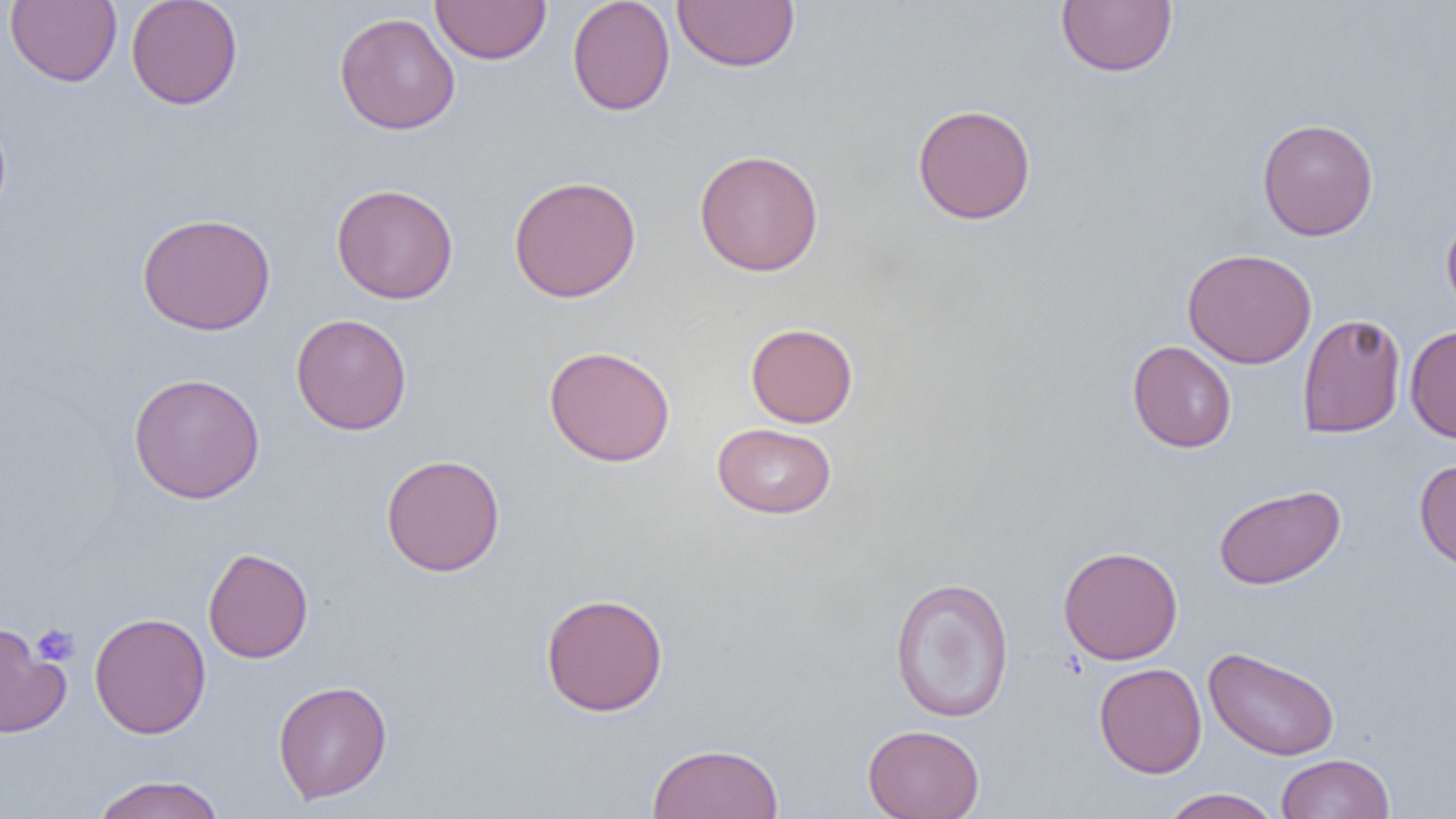
Summary:
  - Coordinate format: approximate bounding boxes as named x1/y1/x2/y2 corners in pixels
  - Uninfected red blood cell locations: (x1=5, y1=0, x2=122, y2=87), (x1=126, y1=0, x2=243, y2=110), (x1=430, y1=0, x2=551, y2=64), (x1=567, y1=0, x2=676, y2=116), (x1=672, y1=0, x2=800, y2=73), (x1=1056, y1=0, x2=1177, y2=77), (x1=334, y1=12, x2=460, y2=135), (x1=912, y1=103, x2=1037, y2=225), (x1=0, y1=110, x2=12, y2=226), (x1=1257, y1=118, x2=1379, y2=241), (x1=694, y1=149, x2=824, y2=276), (x1=508, y1=175, x2=642, y2=303), (x1=331, y1=184, x2=459, y2=304), (x1=1441, y1=208, x2=1456, y2=321), (x1=136, y1=212, x2=276, y2=335), (x1=1182, y1=248, x2=1317, y2=369), (x1=1297, y1=313, x2=1406, y2=438), (x1=290, y1=314, x2=412, y2=435), (x1=745, y1=322, x2=858, y2=428), (x1=1405, y1=325, x2=1456, y2=443), (x1=1127, y1=340, x2=1237, y2=453), (x1=544, y1=345, x2=675, y2=467), (x1=128, y1=372, x2=266, y2=504), (x1=712, y1=422, x2=837, y2=519), (x1=381, y1=454, x2=505, y2=577), (x1=1414, y1=458, x2=1456, y2=572), (x1=1213, y1=484, x2=1346, y2=590), (x1=1057, y1=545, x2=1184, y2=664), (x1=203, y1=547, x2=313, y2=663), (x1=889, y1=575, x2=1015, y2=723), (x1=540, y1=592, x2=669, y2=717), (x1=89, y1=612, x2=211, y2=739), (x1=0, y1=623, x2=70, y2=738), (x1=1204, y1=646, x2=1341, y2=761), (x1=1094, y1=663, x2=1206, y2=778), (x1=273, y1=680, x2=392, y2=804), (x1=862, y1=724, x2=985, y2=819), (x1=646, y1=742, x2=784, y2=819), (x1=1276, y1=753, x2=1395, y2=819), (x1=91, y1=774, x2=226, y2=819), (x1=1159, y1=788, x2=1282, y2=818)
  - Platelet locations: (x1=32, y1=623, x2=79, y2=667)
  - Slide-level diagnosis: negative for blood parasites
  - Modality: light microscopy
  - Magnification: 1000x
  - Field of view: one of a larger specimen
  - Image size: 1456×819 pixels
  - Preparation: thin blood smear